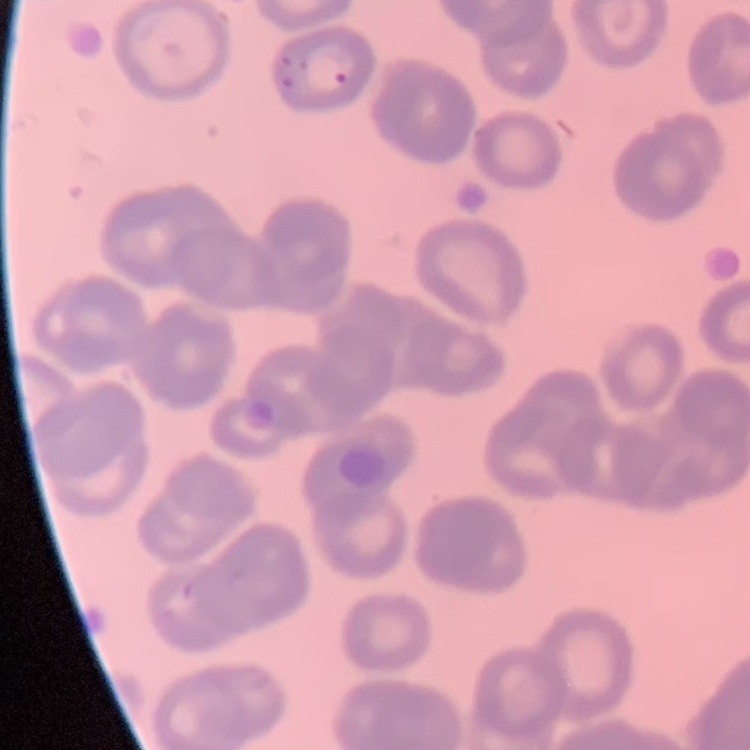
The red blood cells show rouleaux formation. One tile cut from a larger photomicrograph. Field's or Giemsa stain. Thin blood film.